Identify the parasite.
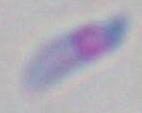
Toxoplasma gondii.

{
  "magnification": "1000x",
  "modality": "photomicrograph"
}